Locate every uninfected red blood cell.
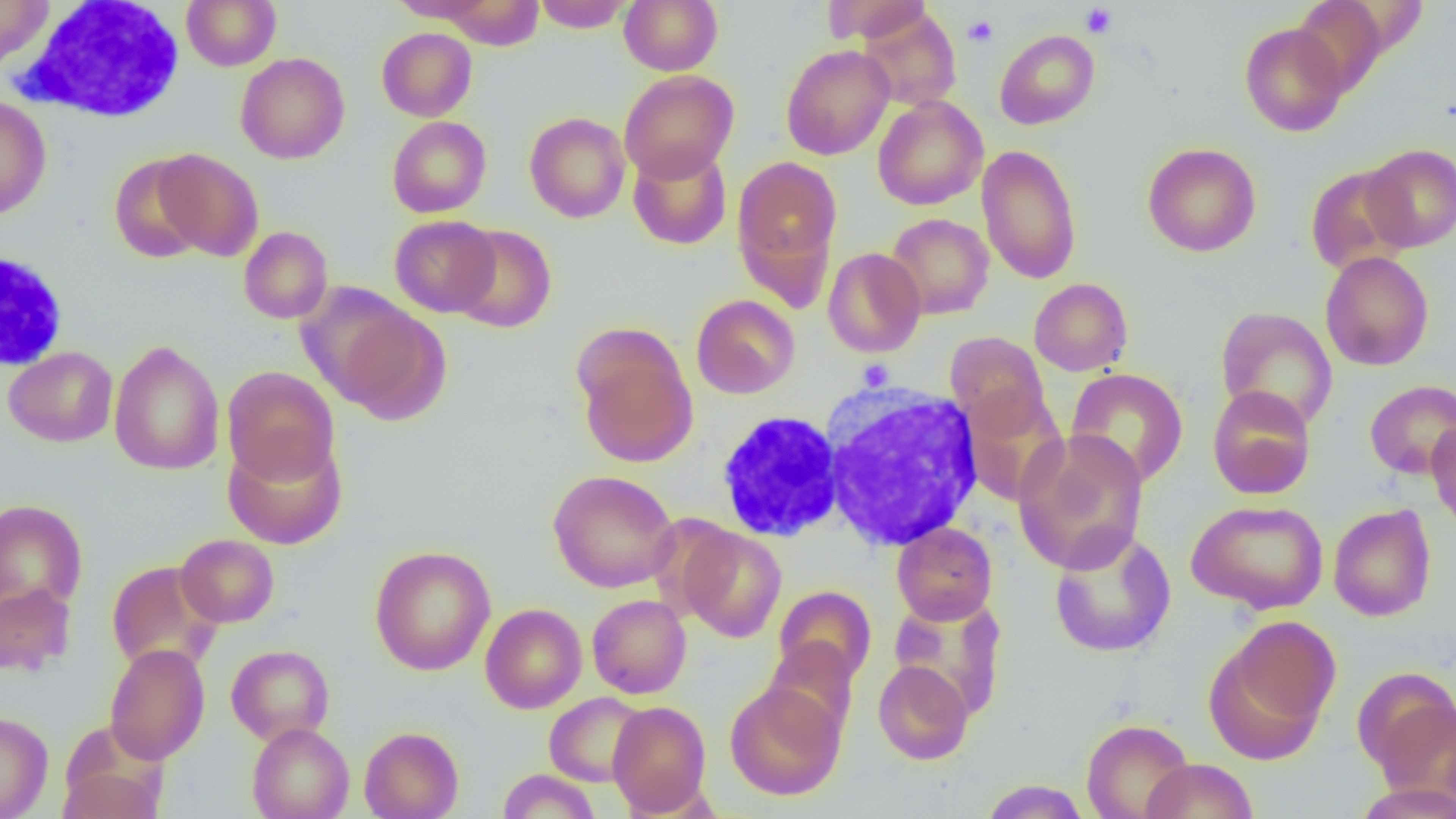

Approximate bounding boxes as (x1,y1)-(x2,y2) corner pairs in pixels.
Uninfected red blood cells (subset): (181,0)-(281,70), (388,0)-(495,24), (439,0)-(544,50), (532,0)-(633,32), (619,0)-(723,75), (822,0)-(932,45), (0,1)-(54,69), (1291,1)-(1391,96), (857,8)-(961,111), (1239,21)-(1349,136), (376,27)-(477,121), (995,29)-(1099,129), (781,44)-(895,160), (235,52)-(350,164), (619,70)-(739,182), (0,95)-(51,219), (873,96)-(988,210), (524,112)-(631,223), (387,116)-(491,218), (1142,142)-(1261,257), (1361,143)-(1456,252), (628,144)-(732,250), (976,144)-(1083,284), (154,148)-(264,260), (109,154)-(211,264), (733,156)-(842,290), (1304,164)-(1413,276), (885,213)-(994,319), (390,215)-(500,317), (449,224)-(556,333), (239,226)-(333,324), (823,247)-(926,357), (1320,251)-(1434,371), (1029,278)-(1133,376), (297,282)-(417,405), (691,294)-(800,399), (333,303)-(451,424), (1214,306)-(1338,431), (945,331)-(1050,432), (577,339)-(698,468), (109,340)-(225,476), (3,346)-(118,447), (222,366)-(340,484), (1065,368)-(1188,488), (1364,380)-(1456,480), (1207,385)-(1316,500), (960,390)-(1069,506), (1426,417)-(1456,535), (1013,429)-(1149,574), (223,434)-(348,549), (548,470)-(679,593), (0,499)-(88,615), (1187,499)-(1329,614), (1328,503)-(1437,621), (892,522)-(997,624), (677,526)-(787,642), (1048,527)-(1177,658), (175,534)-(280,627), (369,545)-(496,675), (106,560)-(222,674), (0,581)-(76,677), (774,586)-(876,686), (587,594)-(691,699), (889,595)-(1007,718), (480,603)-(587,714), (1207,616)-(1341,760), (764,638)-(859,738), (104,643)-(210,765), (226,644)-(335,745), (873,660)-(974,765), (1360,675)-(1455,796), (725,681)-(845,800), (544,692)-(648,786), (607,701)-(711,816), (0,711)-(53,818), (1081,718)-(1195,819), (247,723)-(354,819), (359,726)-(464,818), (1140,758)-(1258,819), (58,762)-(165,819), (497,769)-(600,819), (979,779)-(1091,819), (1355,783)-(1456,819).

slide-level diagnosis = negative for blood parasites
preparation = thin blood smear
field of view = single
image size = 1456×819 pixels
white blood cell locations (subset) = approximate bounding boxes as (x1,y1)-(x2,y2) corner pairs in pixels: (15,0)-(187,124), (0,251)-(70,372), (818,383)-(985,550)
modality = optical microscopy
magnification = 1000x
platelet locations = approximate bounding boxes as (x1,y1)-(x2,y2) corner pairs in pixels: (1080,4)-(1117,38), (962,15)-(999,47), (857,359)-(894,390)